Classify this cell by malaria status.
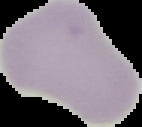
Uninfected.

From a thin blood film. Cell region segmented out of the field of view; the surrounding area is masked to black. Image is 142×127 pixels.